Classify this cell by malaria status.
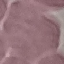

Uninfected.

Summary:
  - Capture: smartphone through the microscope eyepiece
  - Preparation: thin blood film
  - Image type: cell patch, automatically extracted from a larger field of view and resized to 64 × 64 pixels
  - Stain: Giemsa